Evaluate for malaria.
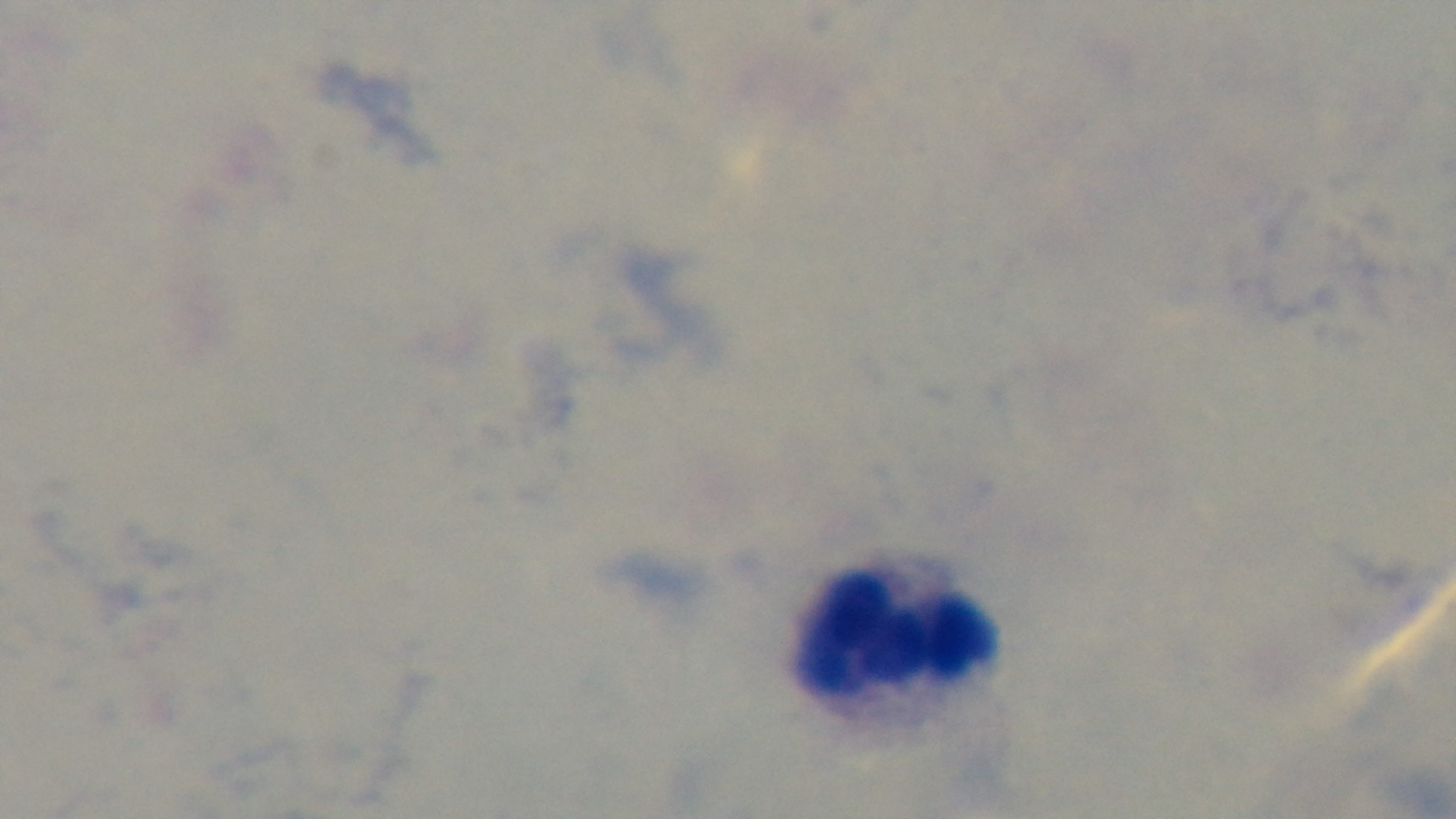

Negative.

Preparation: thick blood film. Photomicrograph. Captured with a mounted 4K digital camera. 100x oil-immersion objective. Single field of view. Giemsa-stained.